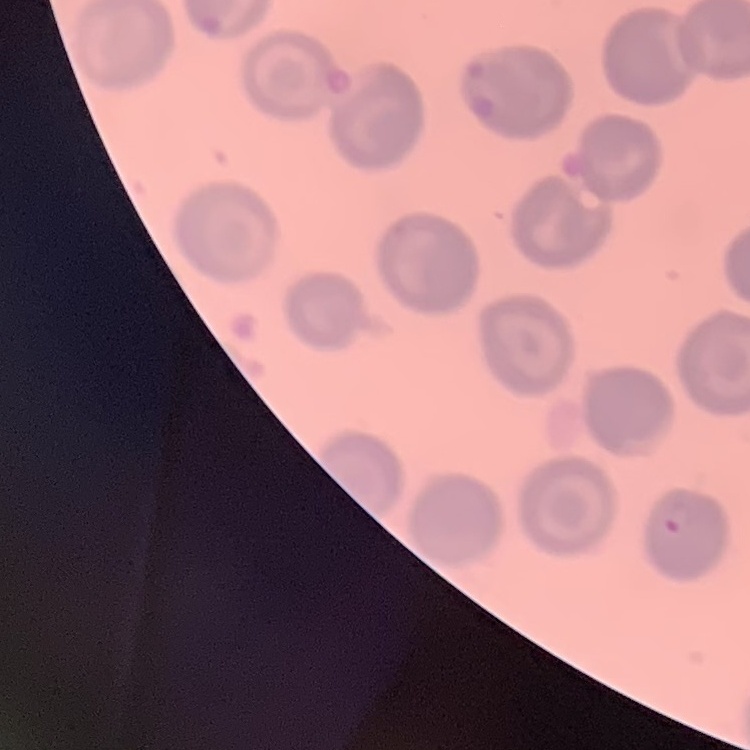
Summary:
  - Erythrocyte morphology: no rouleaux formation
  - Preparation: thin peripheral smear
  - Stain: Field's or Giemsa
  - Image type: square crop of a larger photomicrograph